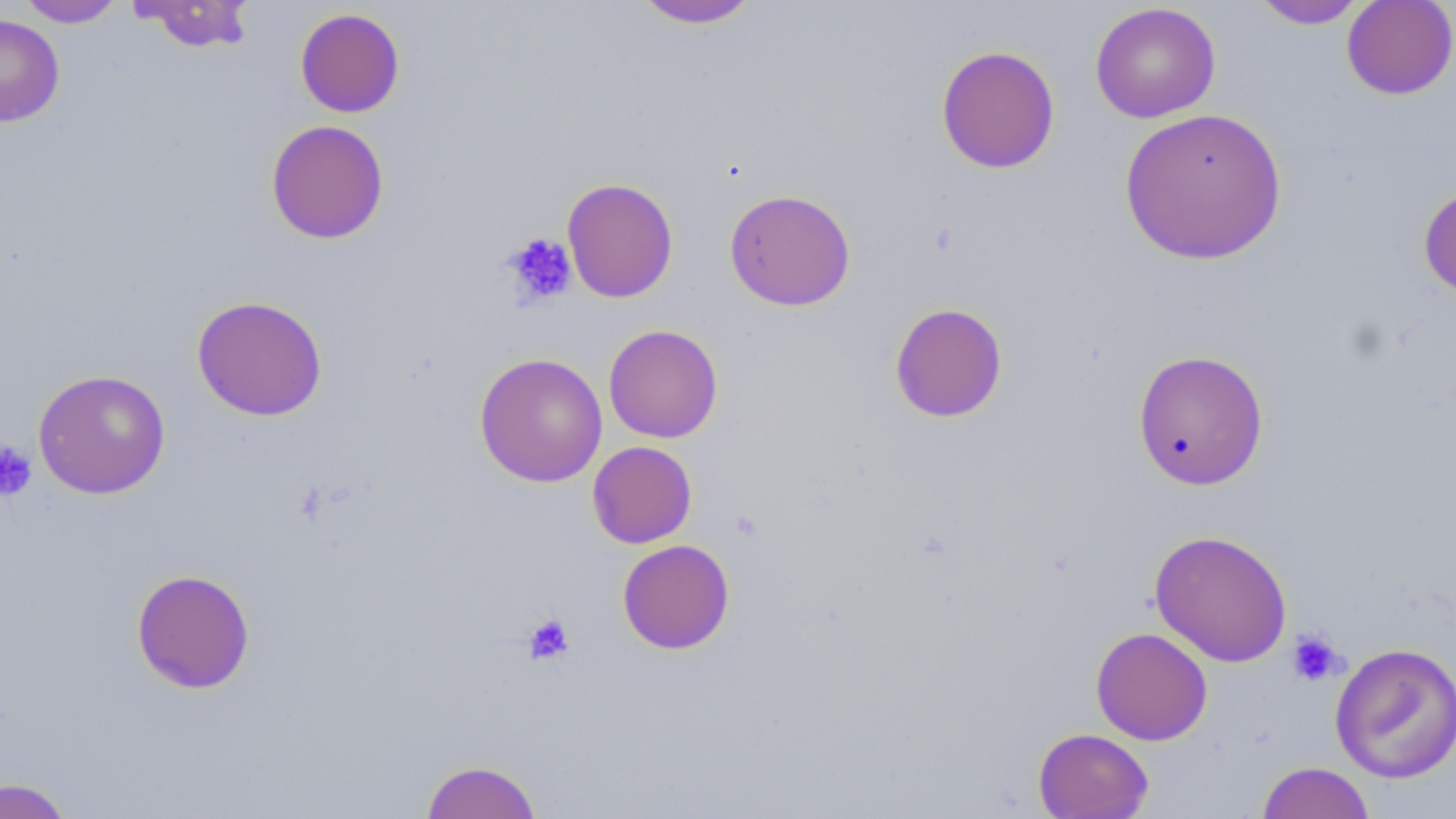
Summary:
  - Coordinate format: approximate bounding boxes as (x1, y1, x2, y2) in pixels
  - Uninfected red blood cell locations: (17, 0, 126, 27), (132, 0, 256, 53), (631, 0, 762, 29), (1341, 0, 1456, 100), (1251, 1, 1370, 29), (1090, 3, 1221, 123), (295, 7, 405, 118), (0, 14, 64, 127), (936, 45, 1060, 174), (1119, 106, 1288, 265), (265, 119, 389, 244), (561, 177, 679, 303), (1418, 183, 1456, 301), (724, 188, 856, 311), (191, 295, 328, 421), (889, 302, 1008, 422), (603, 324, 723, 443), (1131, 348, 1269, 491), (474, 352, 608, 488), (33, 369, 171, 499), (587, 441, 697, 548), (1149, 529, 1293, 667), (617, 539, 735, 654), (131, 568, 255, 693), (1090, 627, 1213, 745), (1330, 642, 1456, 783), (1033, 727, 1154, 818), (421, 759, 542, 818), (1256, 761, 1376, 819), (0, 777, 75, 819)
  - Platelet locations: (502, 233, 578, 307), (0, 441, 37, 501), (521, 613, 574, 665), (1286, 628, 1345, 686)
  - Slide-level diagnosis: no evidence of blood parasites
  - Image size: 1456×819 pixels
  - Modality: light microscopy
  - Magnification: 1000x
  - Field of view: one of a larger specimen
  - Preparation: thin blood film
  - Stain: May-Grünwald-Giemsa